Classify this cell by malaria status.
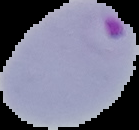
Parasitized.

Summary:
  - Image size: 139×130 pixels
  - Preparation: thin blood film
  - Image type: cell region segmented out of the field of view; surrounding area masked to black